Give the extent of all uninfected red blood cells.
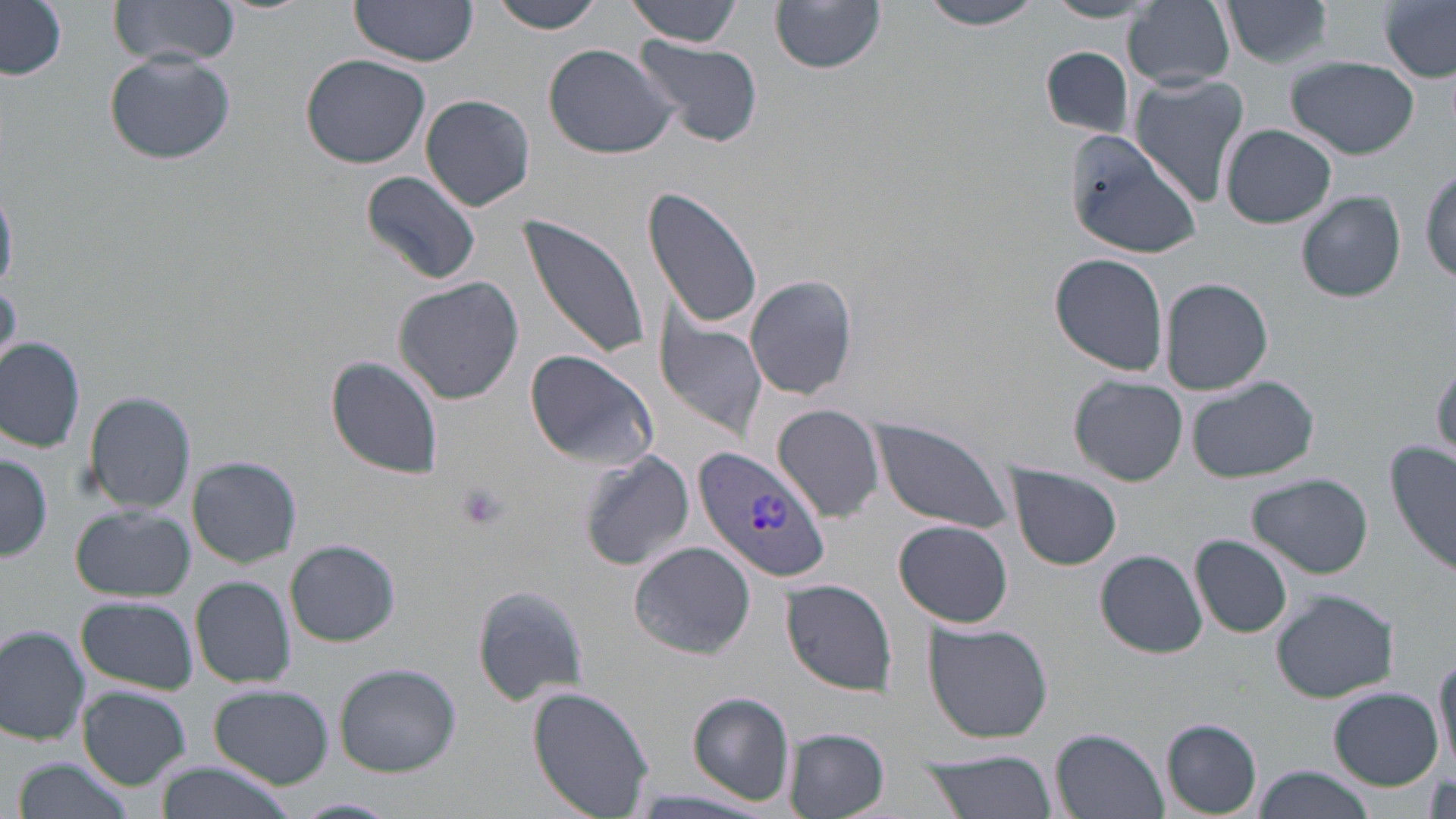
Approximate bounding boxes as (x1, y1, x2, y2) in pixels.
Uninfected red blood cells: (109, 0, 241, 65), (348, 0, 480, 65), (486, 0, 610, 34), (626, 0, 743, 44), (917, 0, 1046, 30), (1377, 0, 1455, 81), (771, 1, 886, 74), (1042, 1, 1158, 23), (1124, 1, 1235, 89), (1220, 1, 1332, 69), (2, 2, 68, 80), (630, 37, 765, 150), (543, 43, 680, 161), (1040, 46, 1134, 140), (105, 50, 236, 166), (301, 54, 432, 170), (1287, 55, 1419, 159), (1128, 74, 1249, 205), (420, 95, 533, 211), (1220, 124, 1336, 230), (1064, 131, 1202, 258), (1420, 165, 1455, 289), (362, 172, 481, 286), (642, 185, 763, 331), (1296, 191, 1406, 303), (518, 214, 650, 363), (1049, 252, 1169, 376), (742, 274, 861, 402), (393, 277, 524, 405), (1162, 279, 1273, 395), (0, 281, 19, 374), (654, 317, 769, 442), (0, 338, 85, 452), (522, 349, 659, 469), (326, 355, 445, 480), (1429, 360, 1456, 460), (1070, 376, 1187, 486), (1188, 376, 1318, 484), (83, 390, 196, 515), (773, 405, 885, 526), (868, 419, 1014, 533), (1386, 443, 1456, 580), (577, 448, 694, 572), (0, 451, 53, 563), (187, 456, 301, 569), (1007, 464, 1123, 571), (1247, 472, 1374, 580), (70, 506, 194, 601), (894, 519, 1015, 629), (1190, 533, 1294, 639), (285, 540, 401, 647), (628, 542, 758, 660), (1097, 549, 1207, 658), (190, 576, 295, 690), (781, 580, 897, 693), (472, 584, 595, 707), (1272, 589, 1399, 702), (77, 597, 198, 694), (924, 622, 1054, 743), (0, 624, 92, 746), (1431, 654, 1456, 773), (333, 662, 462, 776), (210, 686, 335, 787), (525, 686, 657, 816), (1328, 686, 1444, 790), (77, 687, 191, 789), (686, 693, 794, 804), (1162, 719, 1262, 815), (784, 728, 889, 818), (1051, 729, 1168, 818), (915, 749, 1058, 819), (11, 755, 134, 819), (153, 764, 297, 819), (1252, 765, 1378, 819), (624, 786, 778, 818), (284, 797, 402, 819).

Plasmodium vivax-infected red blood cell locations = approximate bounding boxes as (x1, y1, x2, y2) in pixels: (696, 442, 830, 583)
slide-level diagnosis = Plasmodium vivax
image size = 1456×819 pixels
platelet locations = approximate bounding boxes as (x1, y1, x2, y2) in pixels: (454, 481, 509, 531)
modality = light microscopy
stain = May-Grünwald-Giemsa
field of view = single
magnification = 1000x
preparation = thin blood film